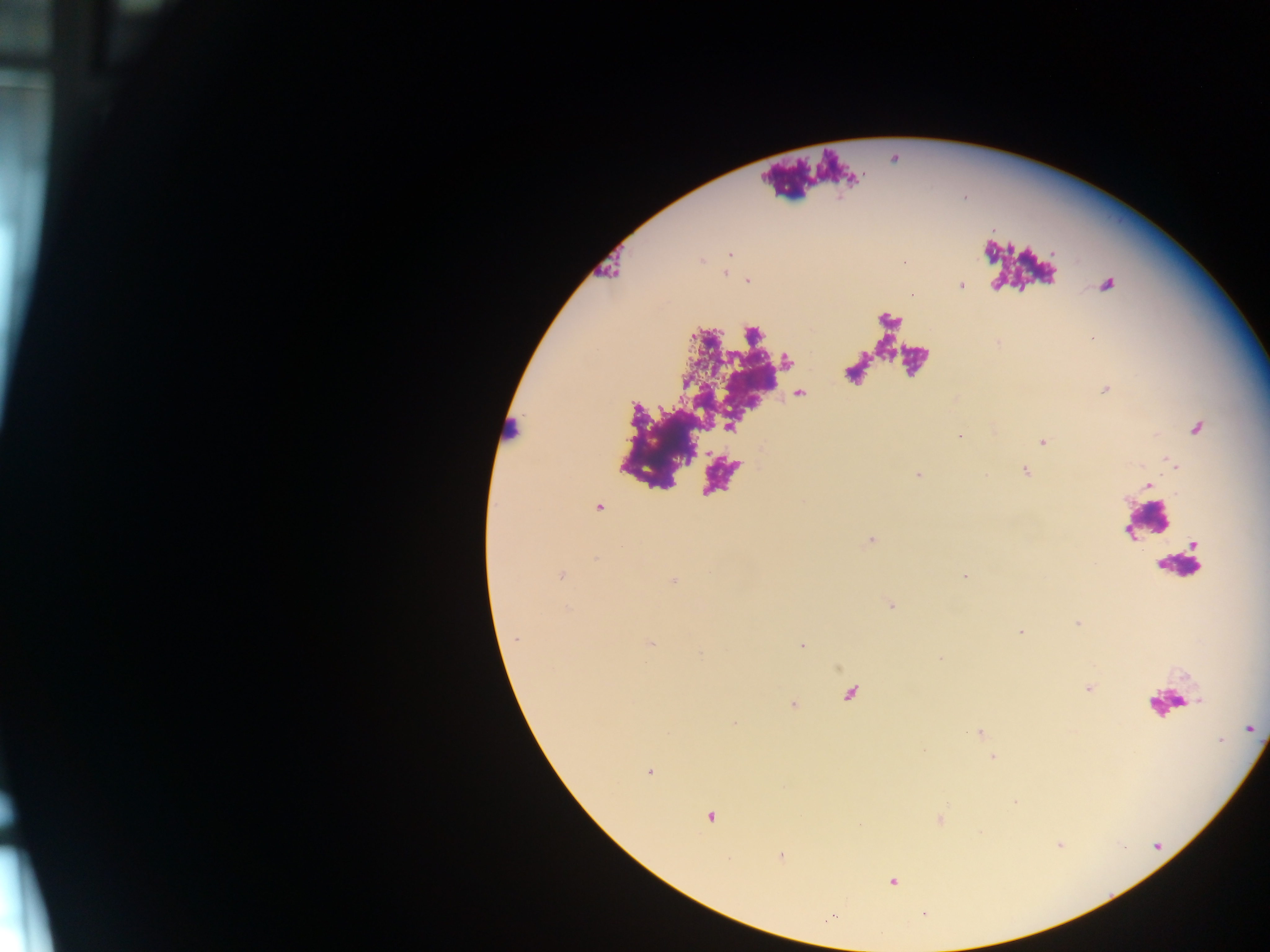

leukocyte_locations: 'approximate centers as x y in pixels: 512 430; 1148 523; 1179 565'
image_size: 1270×952 pixels
country: Ghana
plasmodium_parasite_locations: 'approximate centers as x y in pixels: 747 281; 961 285; 1107 285; 1106 389; 1196 429; 961 437; 1043 442; 1170 462; 1026 471; 918 476; 1148 485; 561 575; 965 577; 674 580; 1021 631; 516 638; 651 643; 1251 728; 1221 740; 649 771; 710 816; 781 856; 892 881'
capture: mobile-phone photograph through a microscope
field_of_view: single
preparation: thick blood smear